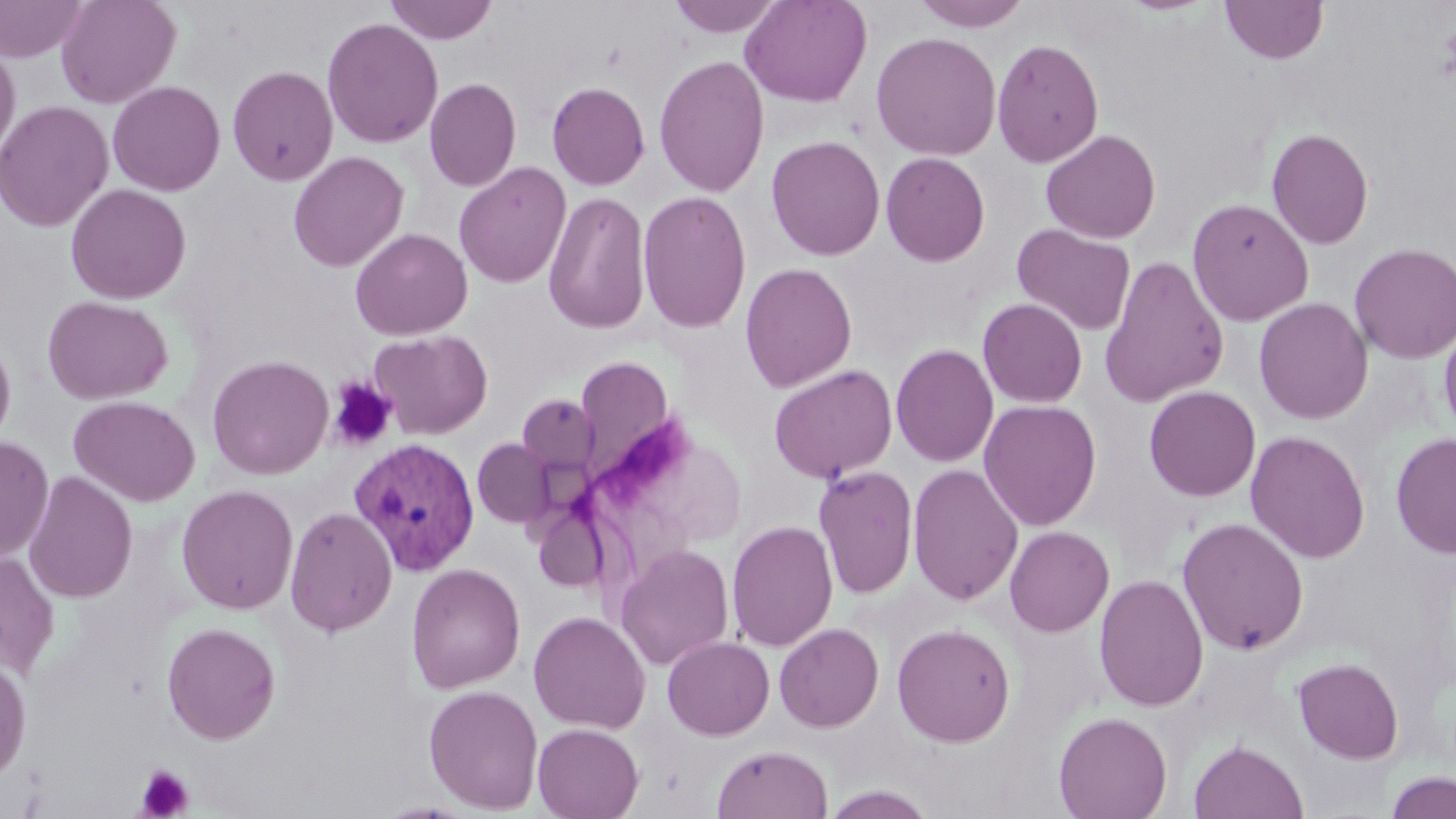

slide_level_diagnosis: Plasmodium vivax
modality: optical microscopy
field_of_view: one of a larger specimen
stain: May-Grünwald-Giemsa
plasmodium_vivax_infected_red_blood_cell_locations: 'approximate bounding boxes as (x1, y1, x2, y2) in pixels: (348, 437, 481, 577)'
image_size: 1456×819 pixels
uninfected_red_blood_cell_locations: 'approximate bounding boxes as (x1, y1, x2, y2) in pixels: (55, 0, 181, 109), (385, 0, 499, 45), (666, 0, 787, 37), (739, 0, 873, 108), (911, 0, 1033, 31), (0, 1, 91, 63), (1220, 1, 1328, 65), (322, 17, 444, 149), (870, 32, 1002, 161), (991, 38, 1105, 167), (0, 42, 20, 161), (654, 54, 770, 198), (227, 65, 339, 186), (424, 77, 521, 192), (107, 80, 226, 196), (547, 81, 650, 190), (0, 100, 114, 232), (1266, 127, 1374, 250), (1040, 129, 1161, 244), (766, 135, 885, 261), (288, 151, 409, 273), (881, 152, 990, 266), (453, 161, 572, 289), (66, 183, 191, 304), (543, 190, 651, 335), (638, 190, 752, 333), (1187, 197, 1314, 327), (1012, 223, 1136, 337), (350, 228, 473, 340), (1349, 242, 1456, 364), (1100, 255, 1228, 408), (740, 262, 857, 392), (42, 295, 173, 405), (1253, 297, 1374, 425), (977, 298, 1087, 408), (1439, 319, 1456, 444), (369, 329, 493, 439), (0, 330, 16, 450), (890, 343, 999, 468), (206, 354, 334, 480), (575, 355, 675, 476), (769, 364, 897, 483), (1144, 385, 1261, 502), (517, 394, 599, 474), (69, 395, 201, 507), (978, 399, 1102, 531), (1245, 430, 1370, 564), (1391, 432, 1456, 560), (0, 436, 54, 561), (473, 438, 554, 529), (907, 463, 1024, 606), (813, 465, 919, 598), (23, 471, 138, 603), (176, 484, 299, 615), (285, 506, 397, 637), (1176, 517, 1309, 656), (726, 520, 838, 652), (1004, 526, 1114, 637), (615, 544, 734, 670), (0, 550, 60, 679), (406, 563, 525, 693), (1094, 574, 1209, 712), (529, 610, 651, 734), (162, 622, 281, 744), (774, 623, 884, 732), (892, 623, 1016, 747), (662, 636, 775, 740), (0, 655, 31, 784), (1292, 657, 1404, 764), (423, 684, 544, 814), (1053, 711, 1173, 819), (532, 723, 644, 819), (1188, 740, 1308, 819), (712, 744, 833, 818), (1384, 770, 1456, 819), (821, 786, 936, 819)'
preparation: thin blood film
platelet_locations: 'approximate bounding boxes as (x1, y1, x2, y2) in pixels: (328, 378, 397, 451), (136, 764, 194, 818)'
magnification: 1000x